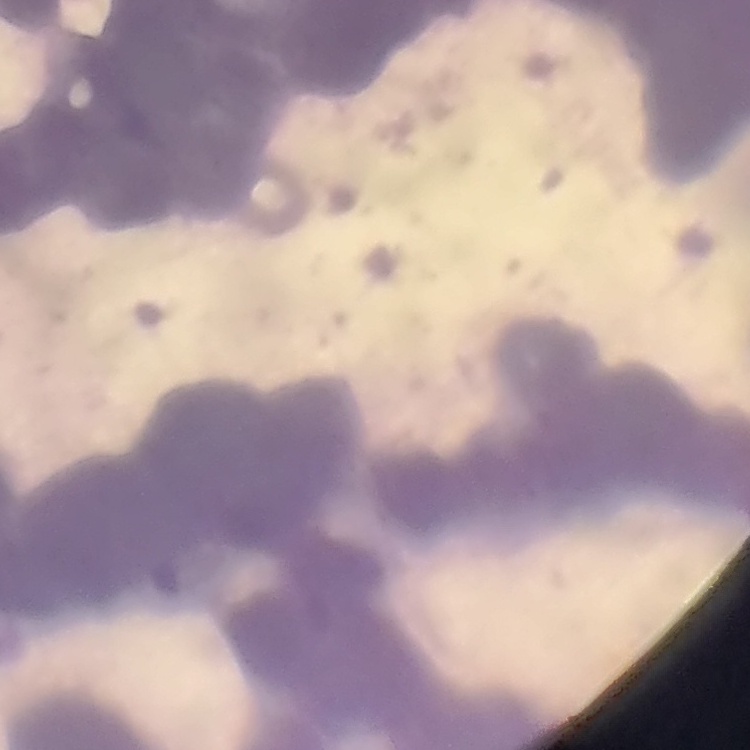 The red blood cells exhibit rouleaux formation. Field's or Giemsa stain. Thin blood film. Square crop of a larger photomicrograph.